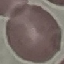

Summary:
  - Result: no malaria parasites detected
  - Capture: smartphone camera at the microscope eyepiece
  - Image type: automatically extracted cell patch, resized to 64 × 64 pixels
  - Preparation: thin smear
  - Stain: Giemsa